Identify the preparation type.
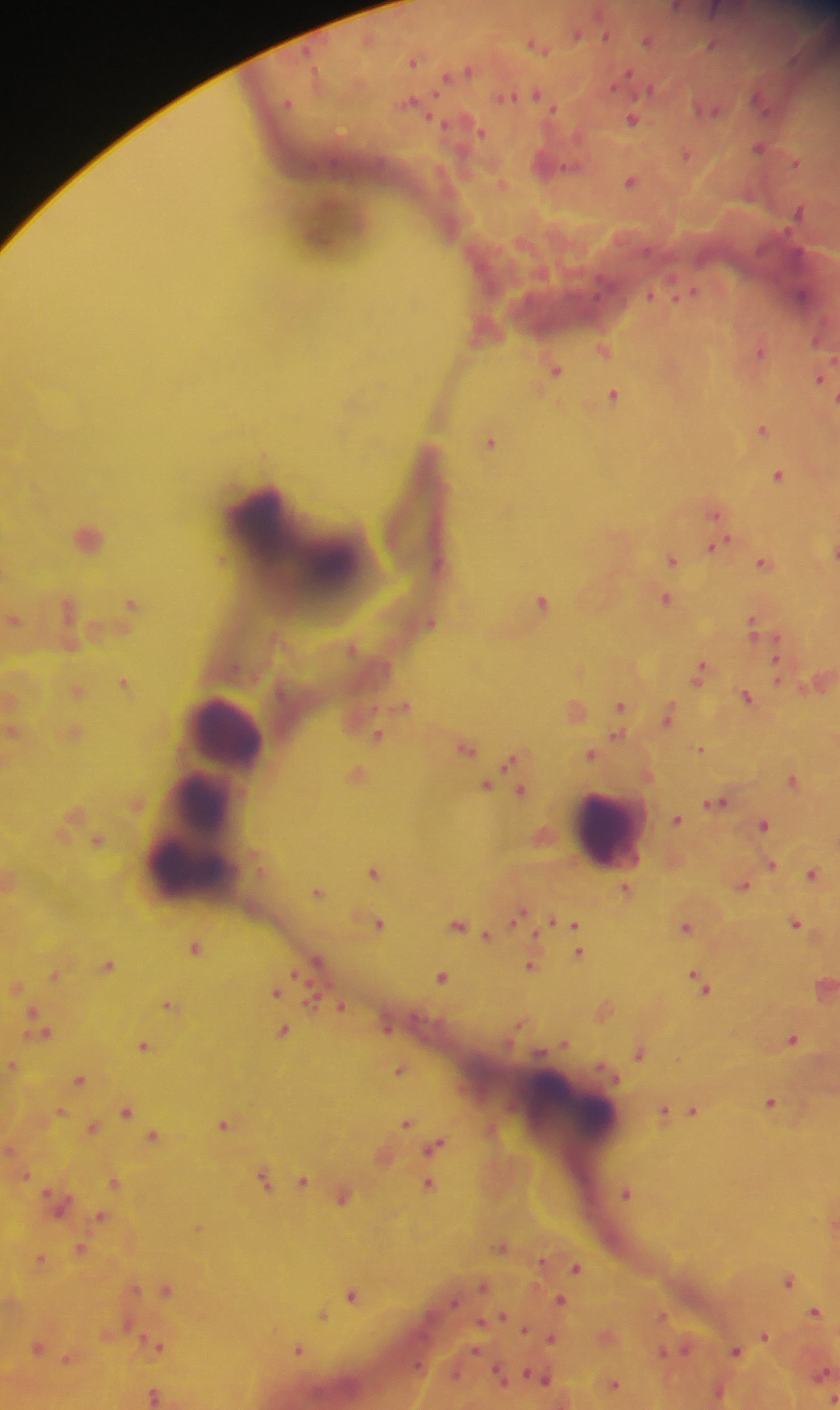

This is a thick smear.

Approximate centers as (x, y) in pixels.
Summary:
  - Leukocyte locations: (330, 225), (262, 520), (221, 732), (202, 803), (199, 819), (606, 833), (188, 864), (572, 1113)
  - Malaria parasite locations: (646, 41), (536, 45), (414, 59), (459, 70), (535, 94), (761, 101), (412, 104), (707, 108), (631, 118), (471, 125), (759, 147), (686, 153), (551, 162), (630, 181), (501, 184), (683, 294), (800, 295), (483, 330), (603, 349), (759, 350), (555, 369), (820, 379), (612, 394), (761, 429), (490, 442), (777, 474), (715, 512), (88, 536), (714, 545), (833, 550), (670, 558), (763, 561), (664, 598), (541, 601), (131, 603), (68, 606), (14, 620), (429, 622), (754, 626), (776, 662), (699, 671), (124, 681), (816, 681), (77, 690), (746, 696), (403, 705), (620, 706), (574, 709), (667, 716), (12, 731), (73, 733), (377, 734), (465, 747), (699, 749), (591, 754), (515, 763), (356, 773), (792, 780), (486, 786), (519, 791), (716, 802), (676, 819), (763, 824), (97, 841), (769, 865), (373, 872), (812, 873), (10, 880), (742, 885), (626, 889), (316, 891), (518, 914), (562, 922), (378, 923), (794, 923), (459, 926), (572, 926), (685, 926), (195, 946), (577, 952), (317, 961), (107, 964), (530, 965), (55, 974), (442, 976), (700, 981), (822, 986), (274, 990), (168, 1004), (338, 1005), (602, 1009), (40, 1025), (282, 1029), (791, 1037), (562, 1043), (143, 1045), (639, 1051), (11, 1065), (399, 1069), (80, 1078), (770, 1102), (126, 1109), (664, 1110), (692, 1110), (60, 1111), (406, 1122), (224, 1123), (93, 1127), (153, 1135), (435, 1145), (382, 1156), (264, 1179), (303, 1179), (114, 1182), (428, 1184), (627, 1192), (343, 1195), (58, 1201), (101, 1217), (198, 1227), (502, 1245), (80, 1248), (40, 1258), (575, 1267), (788, 1278), (482, 1285), (166, 1289), (352, 1295), (560, 1301), (815, 1312), (322, 1314), (606, 1336), (763, 1336), (550, 1338), (156, 1345), (38, 1346), (297, 1349), (674, 1350), (735, 1350), (67, 1358), (822, 1372), (500, 1375), (540, 1376), (613, 1384), (717, 1392), (154, 1394), (832, 1398)
  - Capture: mobile-phone photograph through a microscope
  - Image size: 840×1410 pixels
  - Field of view: single
  - Country: Ghana